Evaluate for Plasmodium parasites.
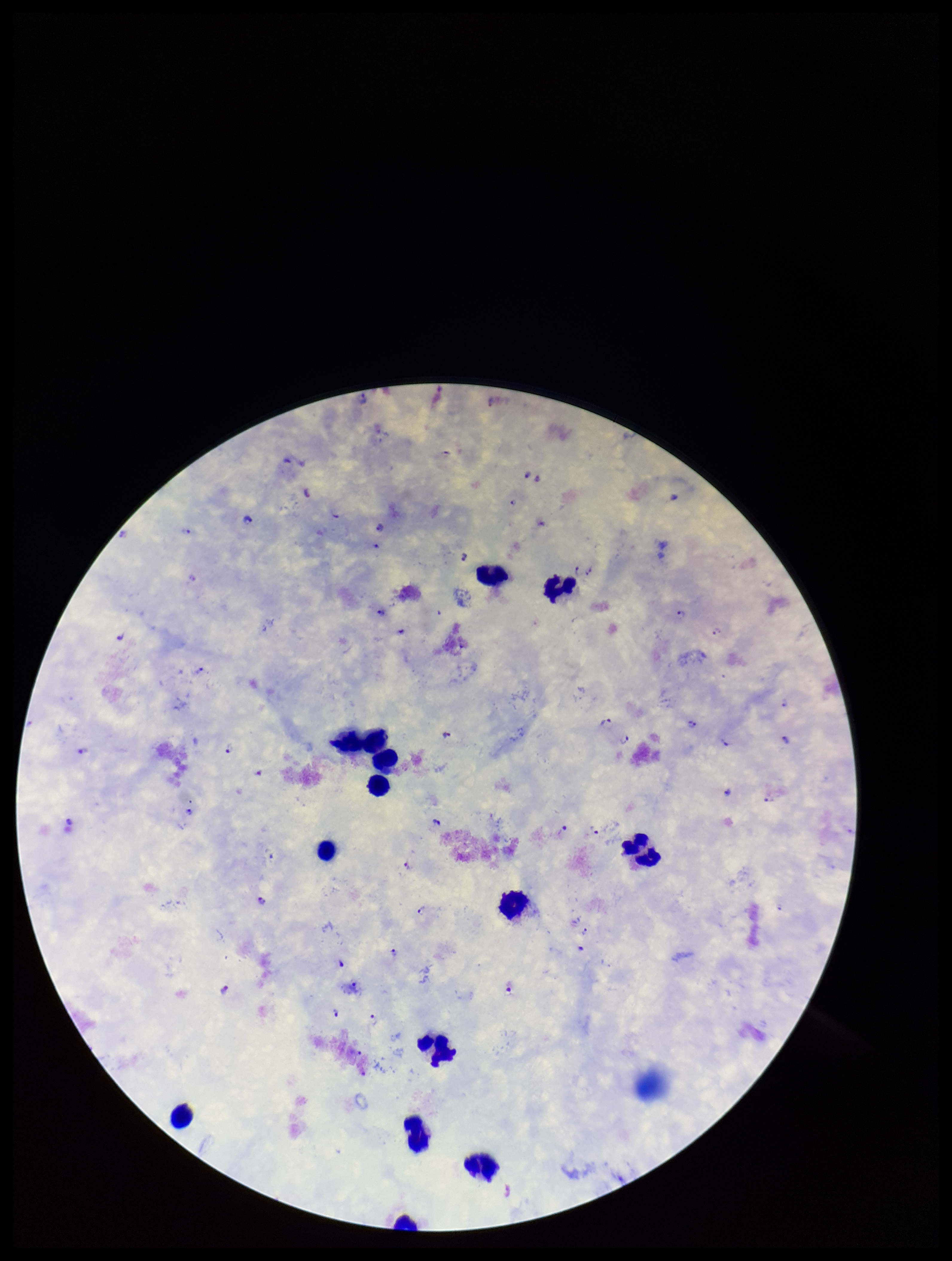

Detected.

Summary:
  - Stain: Giemsa
  - Field of view: one from this slide
  - Species reported for this patient: Plasmodium falciparum
  - Parasite count: 48
  - Image size: 952×1261 pixels
  - Patient malaria status: positive
  - Preparation: thick
  - Capture: smartphone photograph through the microscope eyepiece
  - Leukocyte count: 12